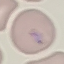

malaria status = parasitized
capture = smartphone through the microscope eyepiece
stain = Giemsa
preparation = thin smear
image type = cell patch, automatically extracted from a larger field of view and resized to 64 × 64 pixels